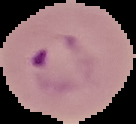

image type = segmented cell region on a black background
preparation = thin blood smear
result = malaria parasites detected
image size = 136×124 pixels